Identify the cell.
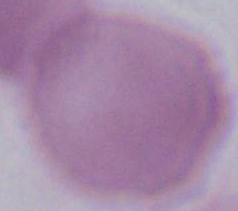

An erythrocyte.

Captured at 1000x magnification. Micrograph.